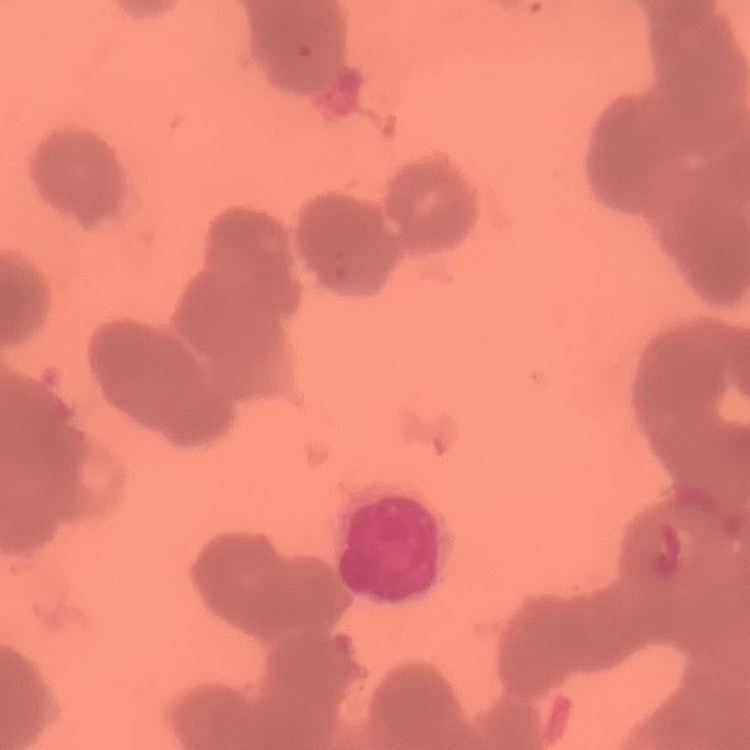

erythrocyte morphology = rouleaux formation
image type = square crop of a larger photomicrograph
preparation = thin blood smear
stain = Field's or Giemsa